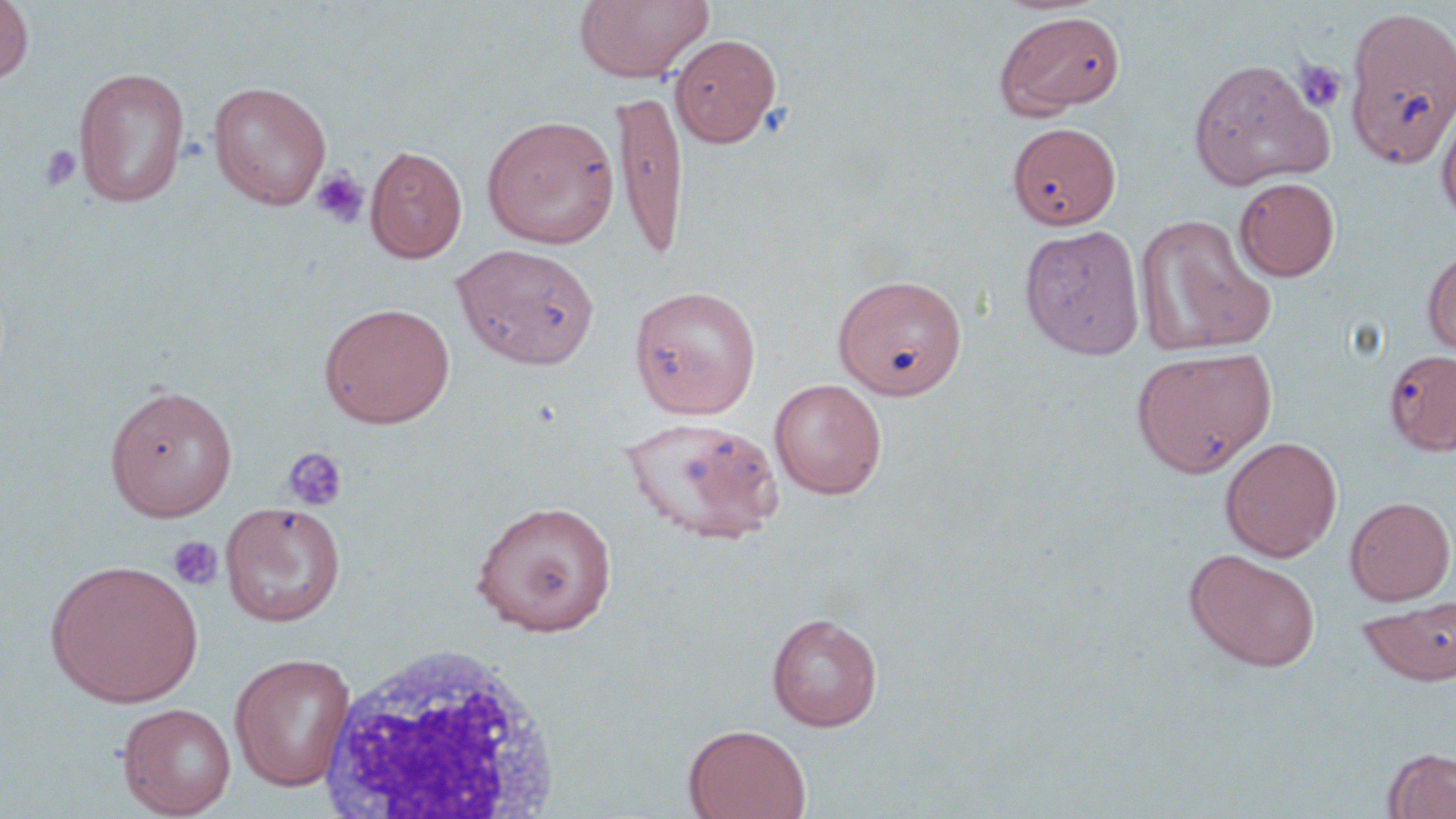
Summary:
  - Coordinate format: approximate bounding boxes as (x1,y1)-(x2,y2) corner pairs in pixels
  - White blood cell locations: (314,643)-(563,817)
  - Platelet locations: (1294,58)-(1348,113), (38,145)-(82,192), (310,167)-(370,229), (282,446)-(348,511), (167,536)-(223,591)
  - Uninfected red blood cell locations: (574,0)-(714,82), (0,1)-(34,83), (1342,5)-(1456,170), (994,10)-(1126,118), (670,34)-(781,147), (1187,58)-(1333,190), (73,66)-(191,208), (207,80)-(332,210), (611,88)-(688,261), (1436,100)-(1456,227), (482,114)-(620,248), (1007,121)-(1121,229), (366,144)-(468,263), (1234,177)-(1340,281), (1135,214)-(1275,358), (1019,224)-(1145,360), (451,244)-(600,370), (1422,246)-(1456,358), (833,273)-(968,400), (629,285)-(762,419), (319,301)-(456,428), (1130,345)-(1277,477), (1384,349)-(1456,455), (769,379)-(887,499), (104,383)-(238,522), (620,416)-(784,545), (1220,436)-(1342,562), (1345,496)-(1455,605), (469,499)-(618,636), (220,501)-(346,627), (1184,548)-(1321,671), (45,558)-(203,707), (1358,595)-(1456,687), (766,611)-(883,731), (229,652)-(356,791), (117,702)-(236,817), (683,723)-(811,818), (1383,747)-(1456,818)
  - Slide-level diagnosis: no evidence of blood parasites
  - Image size: 1456×819 pixels
  - Magnification: 1000x
  - Stain: May-Grünwald-Giemsa
  - Preparation: thin blood smear
  - Modality: optical microscopy
  - Field of view: single